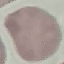
Summary:
  - Result: negative for malaria parasites
  - Image type: automatically extracted cell patch, resized to 64 × 64 pixels
  - Stain: Giemsa
  - Capture: smartphone camera at the microscope eyepiece
  - Preparation: thin blood film